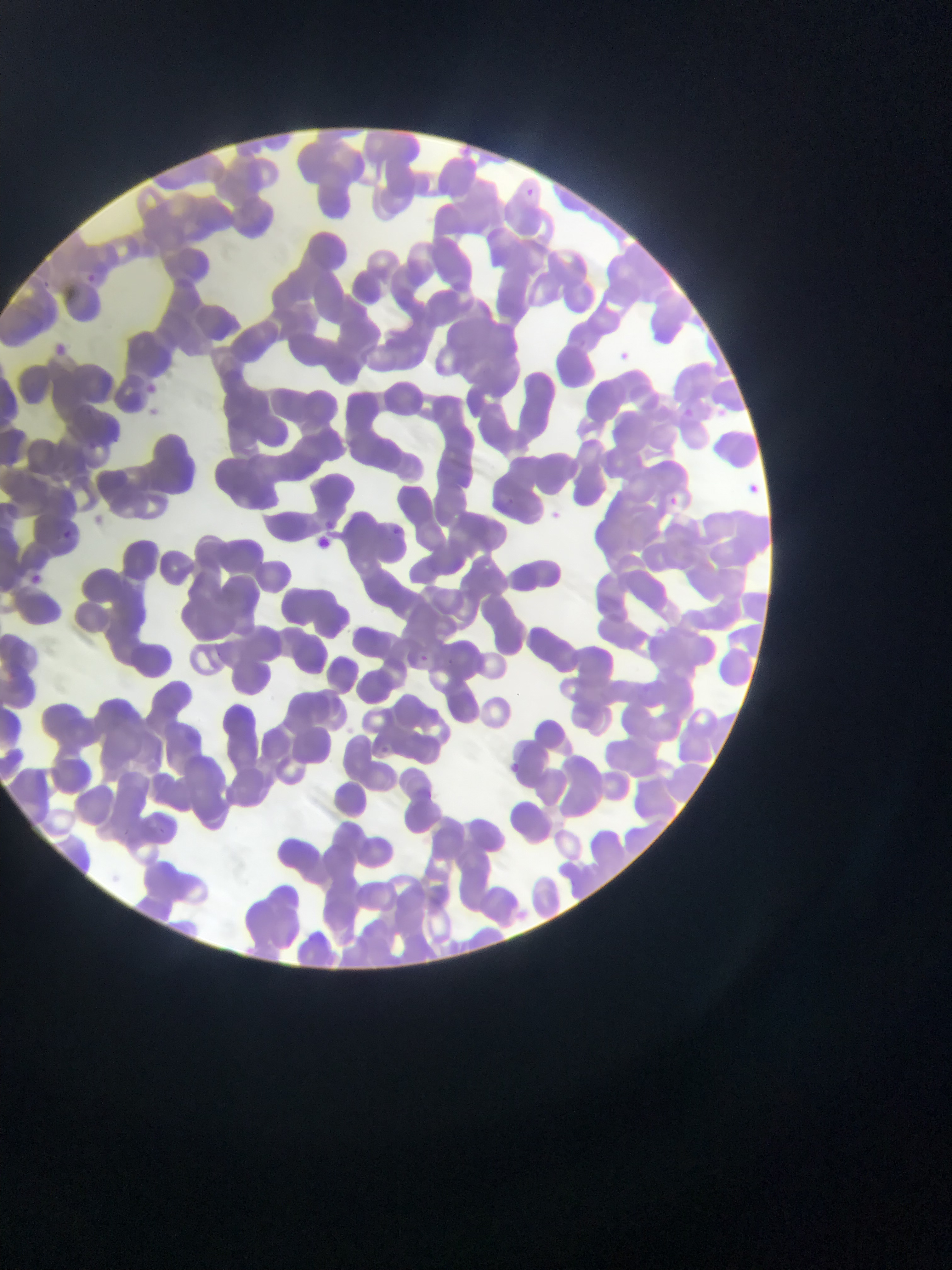
Plasmodium parasite locations = approximate bounding boxes as [left, top, right, bottom] in pixels: [526, 183, 541, 198], [85, 272, 101, 283], [41, 276, 57, 291], [609, 345, 635, 370], [690, 406, 697, 417], [743, 479, 763, 498], [664, 492, 683, 511], [507, 496, 520, 509], [542, 505, 567, 527], [391, 525, 404, 540], [66, 529, 82, 544], [21, 568, 49, 595], [418, 650, 430, 663], [504, 759, 525, 779]
image size = 952×1270 pixels
country = Ghana
field of view = single
capture = mobile-phone photograph through a microscope
preparation = thin blood film